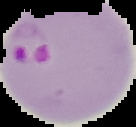
Summary:
  - Malaria status: parasitized
  - Preparation: thin blood smear
  - Image type: cell region segmented out of the field of view; surrounding area masked to black
  - Image size: 136×127 pixels